State which cell type is depicted.
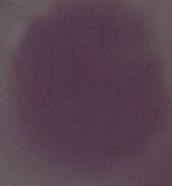
An erythrocyte.

modality: photomicrograph
magnification: 1000x